Report the malaria status of this cell.
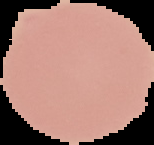
Uninfected.

image_type: cell region segmented out of the field of view; surrounding area masked to black
preparation: thin blood film
image_size: 154×145 pixels